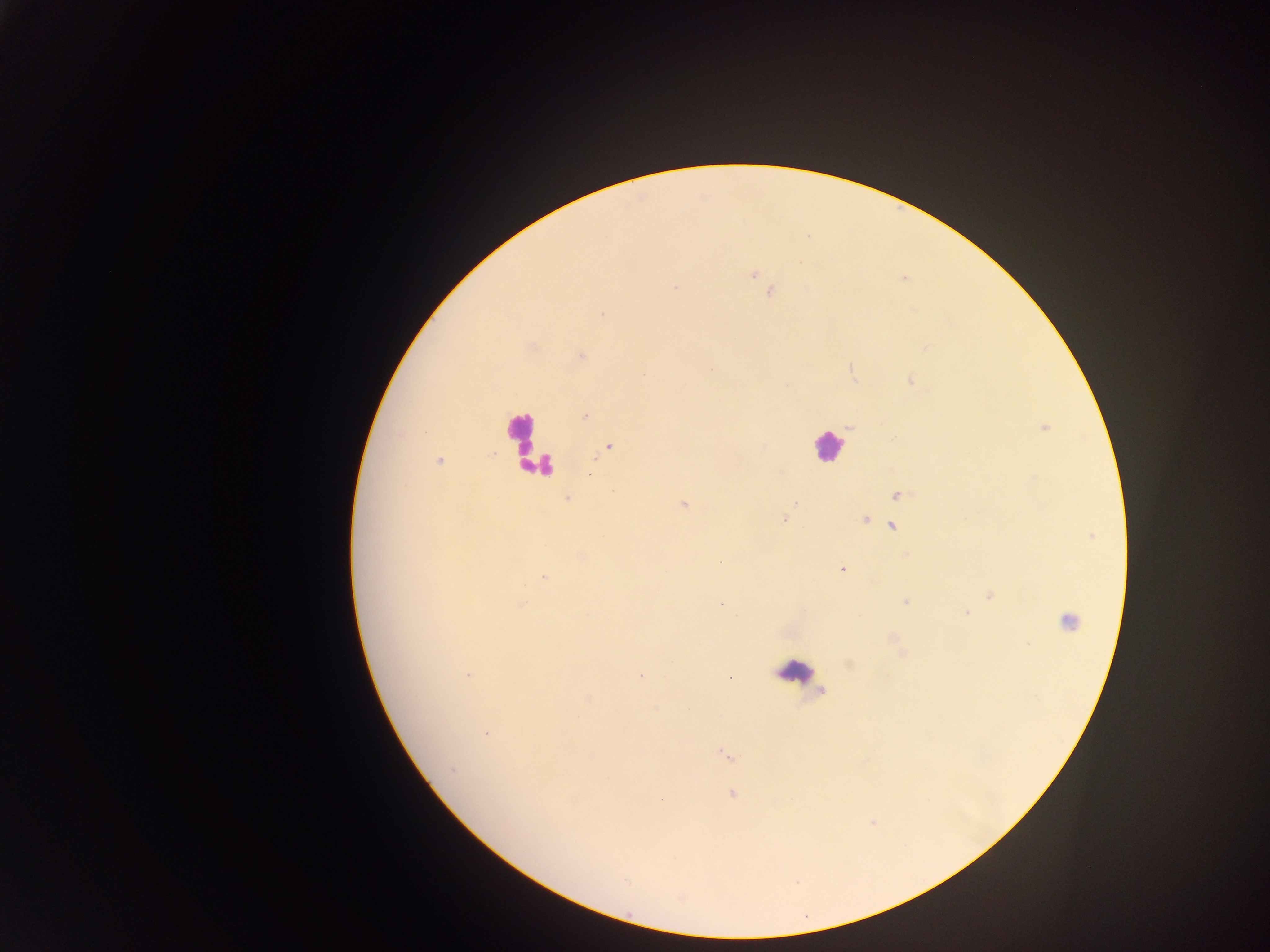

preparation = thick blood smear
leukocyte locations = approximate centers as x y in pixels: 521 436; 828 447; 531 460; 541 465; 1068 621; 792 670
country = Ghana
image size = 1270×952 pixels
Plasmodium parasite locations = approximate centers as x y in pixels: 753 274; 770 291; 601 314; 925 347; 580 355; 852 369; 910 380; 584 416; 849 426; 1043 427; 608 446; 439 461; 897 495; 567 498; 683 503; 797 503; 783 518; 865 518; 892 527; 1091 535; 907 553; 580 555; 720 561; 842 569; 544 577; 990 596; 906 600; 520 604; 720 604; 966 614; 892 637; 902 654; 468 676; 640 676; 730 677; 822 691; 487 733; 726 755; 732 794; 871 821
field of view = single
capture = mobile-phone photograph through a microscope